State which parasite is depicted.
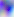
This is Toxoplasma gondii.

magnification = 400x
modality = micrograph